Comment on the morphology of the erythrocytes.
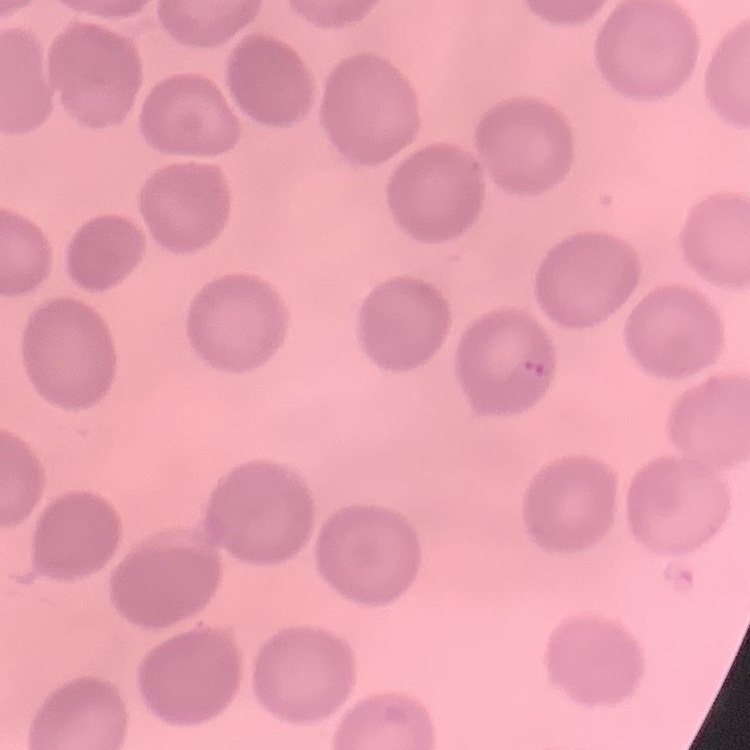
No rouleaux formation.

Field's or Giemsa stain. One tile cut from a larger photomicrograph. Thin blood smear.